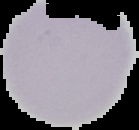
From a thin blood film. Image is 139×130 pixels. Result: no Plasmodium parasites seen. The area outside the segmented cell region is set to black.